Locate every Plasmodium parasite.
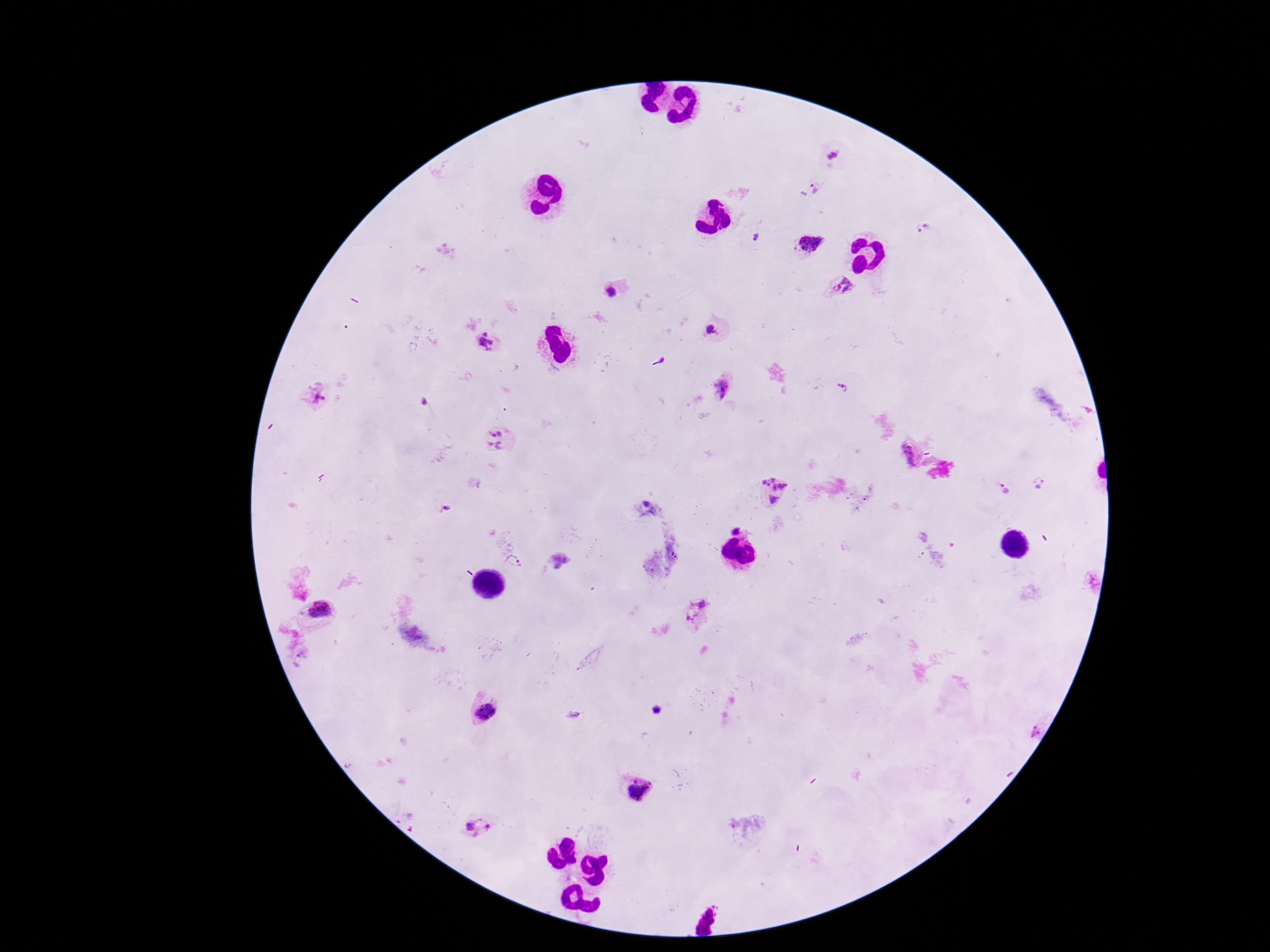

Approximate centers as (x, y) in pixels.
Plasmodium parasites: (833, 156), (817, 187), (922, 230), (757, 235), (811, 245), (842, 286), (610, 293), (710, 330), (486, 342), (722, 387), (842, 388), (318, 398), (497, 439), (909, 452), (1039, 484), (1004, 489), (773, 492), (514, 562), (320, 611), (698, 614), (487, 712), (638, 789), (478, 829).

Summary:
  - Patient malaria status: positive
  - Preparation: thick blood smear
  - Stain: Giemsa
  - Field of view: single
  - Magnification: 100x
  - Image size: 1270×952 pixels
  - Capture: smartphone camera through the microscope eyepiece